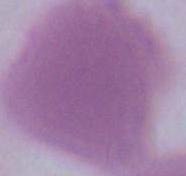
Summary:
  - Modality: photomicrograph
  - Identification: erythrocyte
  - Magnification: 1000x